Identify the parasite.
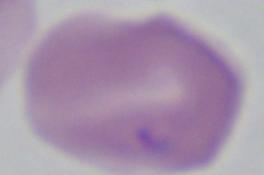

This is Babesia.

1000x magnification. Micrograph.